Evaluate for malaria.
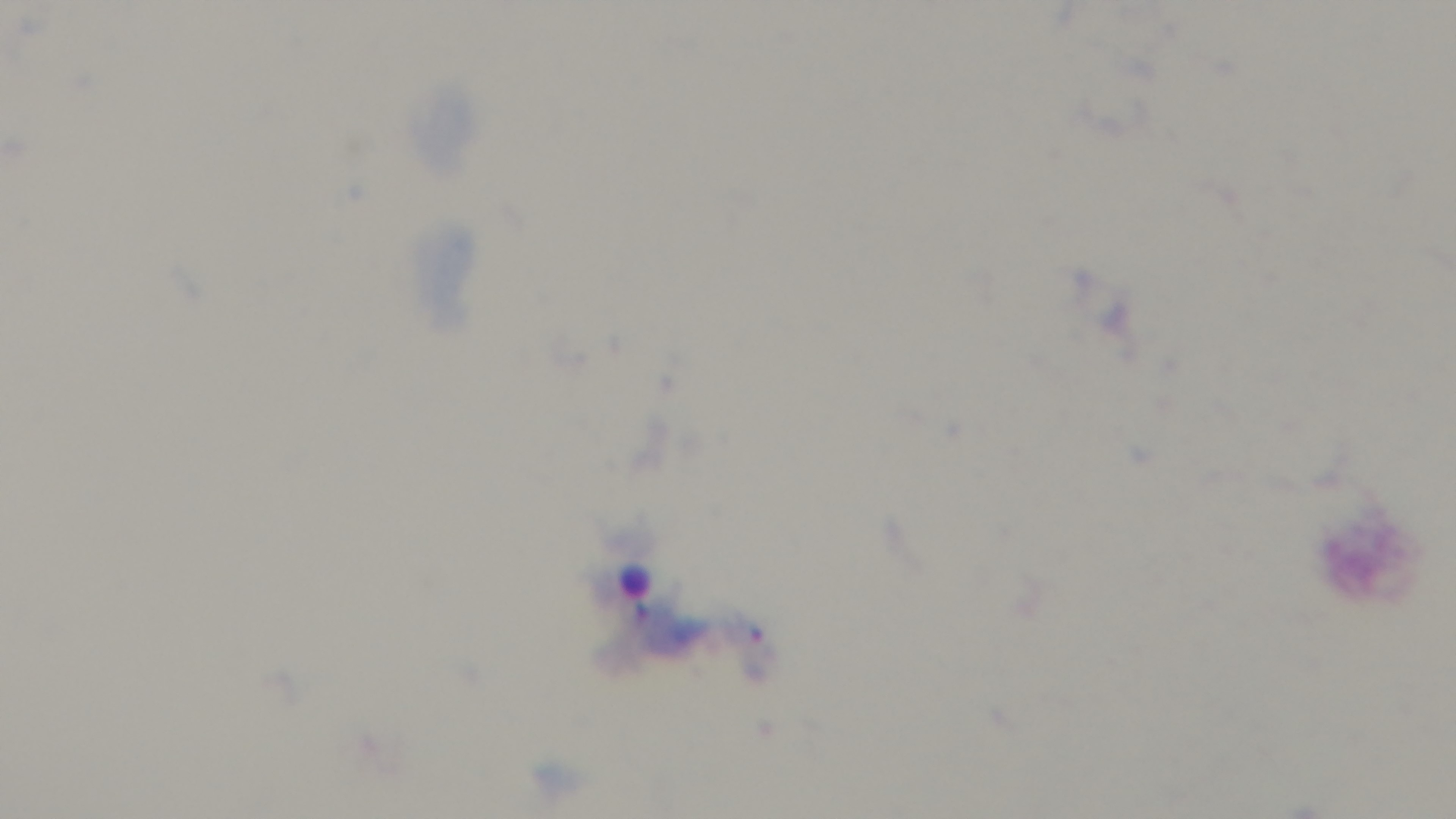

Infected.

Preparation: thick blood film. Giemsa-stained. One field from the slide. Mounted 4K digital camera. Light microscopy. Oil-immersion objective, 100x.